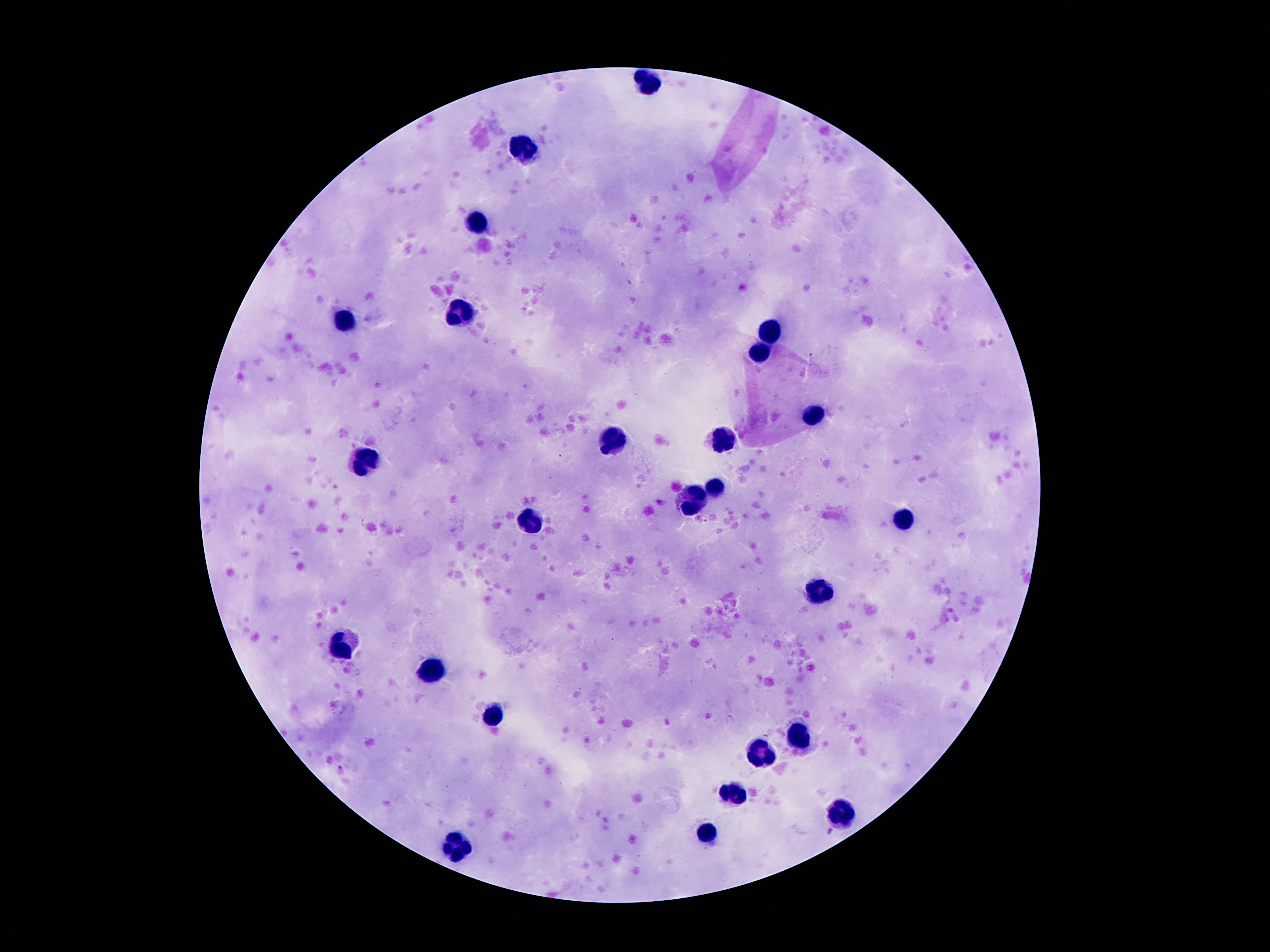
Approximate centers as {x, y} in pixels. Leukocyte locations: {647, 80}, {531, 146}, {477, 222}, {462, 315}, {344, 323}, {773, 328}, {760, 353}, {811, 413}, {723, 440}, {611, 442}, {365, 463}, {712, 488}, {691, 500}, {899, 522}, {531, 523}, {821, 589}, {349, 642}, {433, 670}, {496, 718}, {798, 739}, {763, 754}, {733, 796}, {842, 814}, {708, 838}, {452, 848}. 100x magnification. Single field of view. Photographed through the microscope eyepiece with a smartphone camera. Image is 1270×952 pixels. Giemsa-stained preparation. Thick blood smear. Patient malaria status: uninfected.